Classify this cell by malaria status.
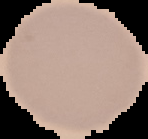
It is uninfected.

Image is 148×139 pixels. From a thin blood smear. Segmented cell region on a black background.